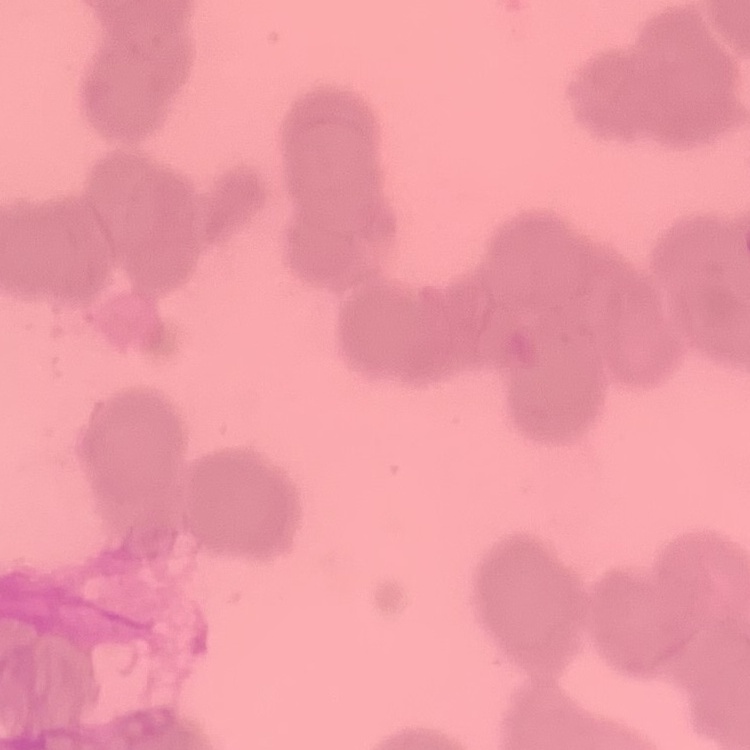
red blood cell morphology = rouleaux formation
stain = Field's or Giemsa
preparation = thin blood smear
image type = one tile cut from a larger photomicrograph